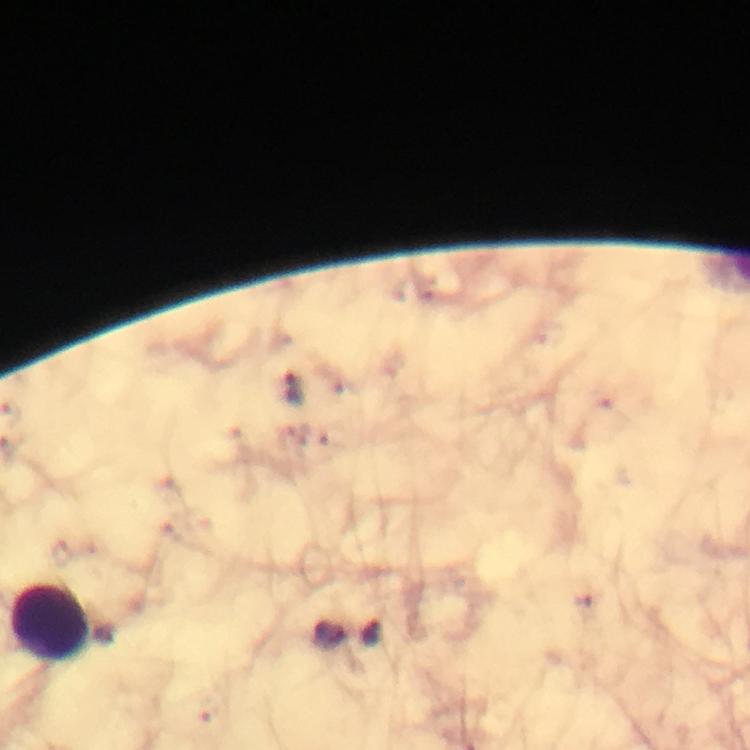 Approximate object centers, in pixels from the top-left corner. Leukocyte locations: (x=51, y=623). Plasmodium parasite locations: (x=294, y=388), (x=580, y=603), (x=327, y=635), (x=374, y=635). Cropped region of a single field of view. Photographed with a smartphone mounted on the microscope. Immersion oil applied. 100x magnification. Image is 750×750 pixels. Giemsa stain. Thick blood smear. From a diagnostic examination for malaria.